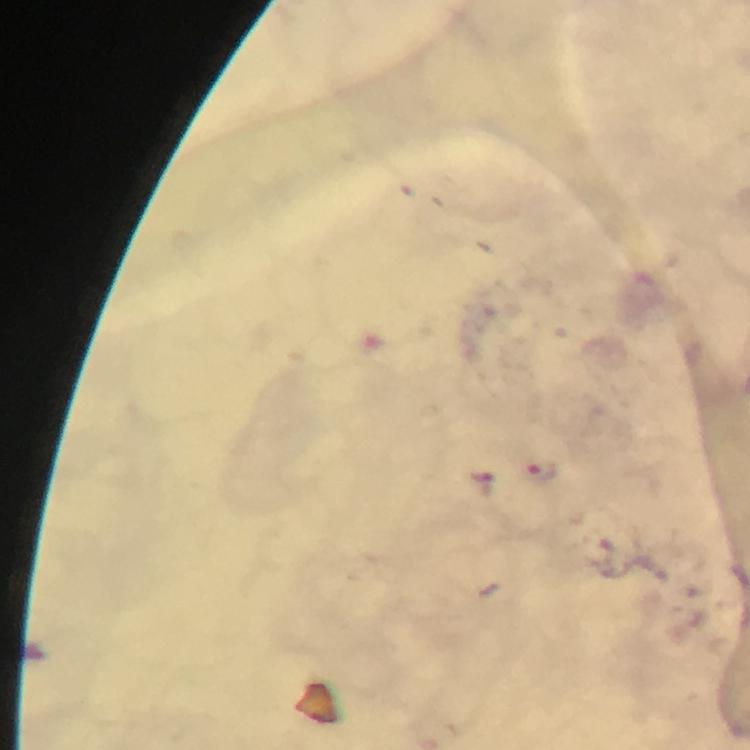
Approximate centers as [x, y] in pixels.
Summary:
  - Malaria parasite locations: [540, 472]
  - Stain: Giemsa
  - Capture: smartphone camera through the microscope
  - Immersion oil: applied
  - Image size: 750×750 pixels
  - Preparation: thick blood film
  - Magnification: 100x
  - Cropped from: one field of view
  - Context: from a diagnostic examination for malaria